State the preparation type.
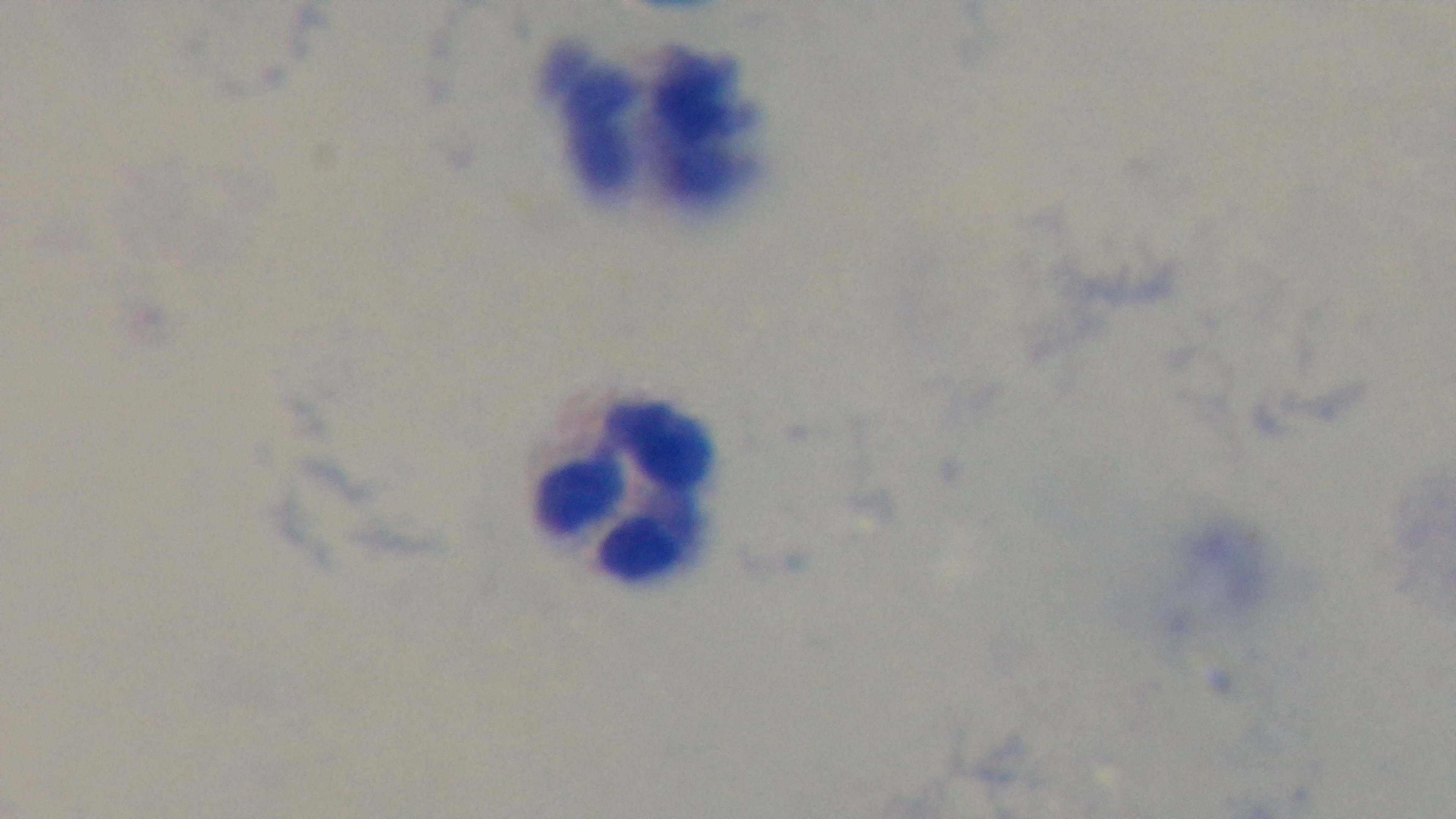
It is a thick blood film.

Summary:
  - Modality: light microscopy
  - Malaria status: negative
  - Stain: Giemsa
  - Field of view: one from the slide
  - Capture: mounted 4K digital camera
  - Objective: 100x oil immersion